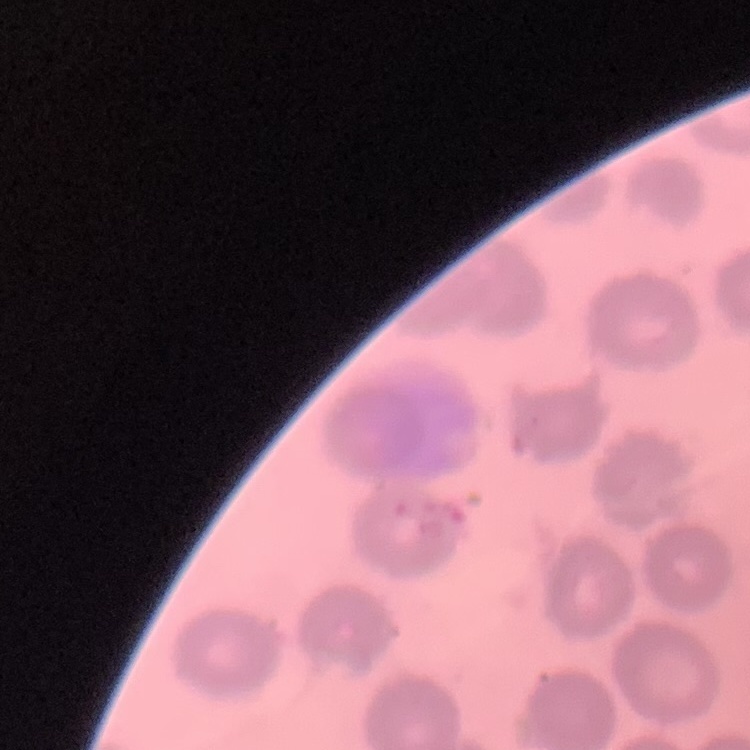

The red blood cells exhibit no rouleaux formation. Stained with either Field's or Giemsa. Thin blood smear. Square crop of a larger photomicrograph.